Name the cell type shown.
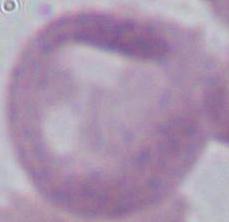

An erythrocyte.

Captured at 1000x magnification. Photomicrograph.